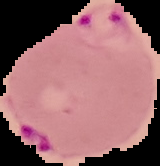

{
  "preparation": "thin blood film",
  "result": "Plasmodium parasites identified",
  "image_type": "segmented cell region with the area outside set to black",
  "image_size": "160×166 pixels"
}